Assess this cell for malaria.
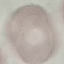

It is uninfected.

Thin smear of blood. Automatically extracted cell patch, resized to 64 × 64 pixels. Photographed with a smartphone camera at the microscope eyepiece. Giemsa stain.